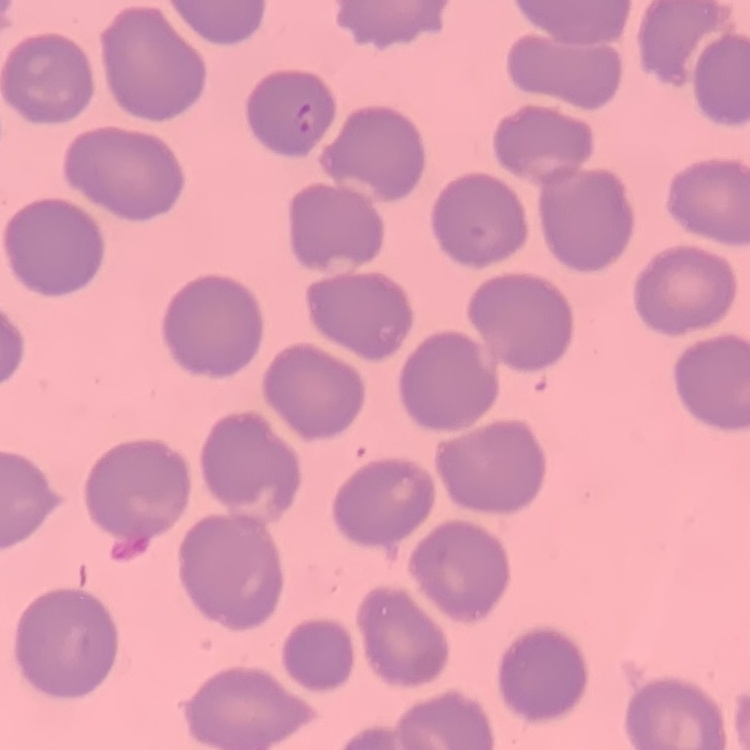
Summary:
  - Red blood cell morphology: no rouleaux formation
  - Stain: Field's or Giemsa
  - Image type: one tile cut from a larger photomicrograph
  - Preparation: thin peripheral smear